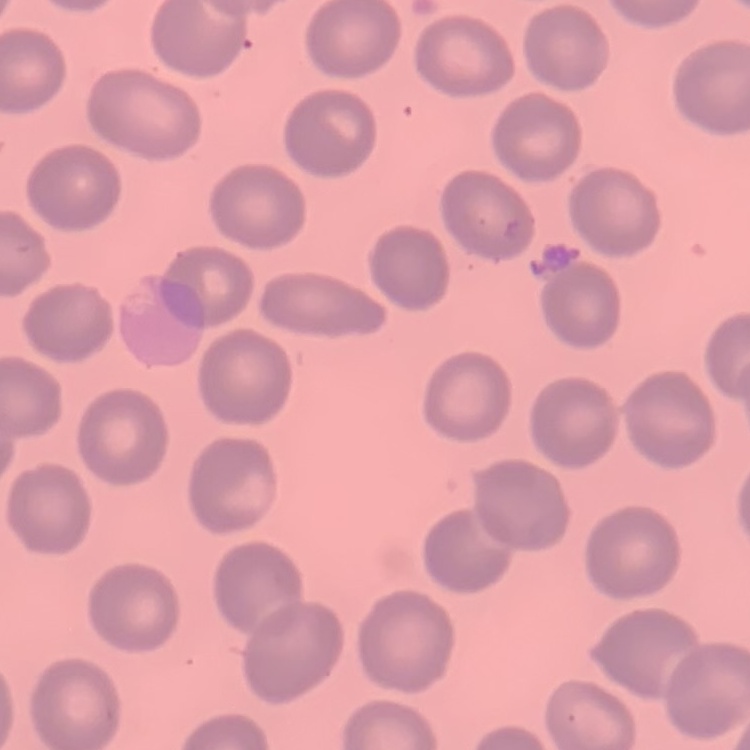 The erythrocytes show no rouleaux formation. One tile cut from a larger photomicrograph. Stained with either Field's or Giemsa. Thin blood smear.